Classify this cell by malaria status.
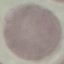

Uninfected.

Cell patch, automatically extracted from a larger field of view and resized to 64 × 64 pixels. Giemsa-stained preparation. Thin blood film. Photographed with a smartphone camera at the microscope eyepiece.